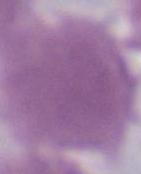

An erythrocyte is seen. 1000x magnification. Photomicrograph.